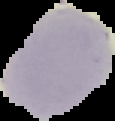

image size = 115×121 pixels
preparation = thin blood film
image type = cell region segmented out of the field of view; surrounding area masked to black
malaria status = uninfected